Look for Plasmodium parasites.
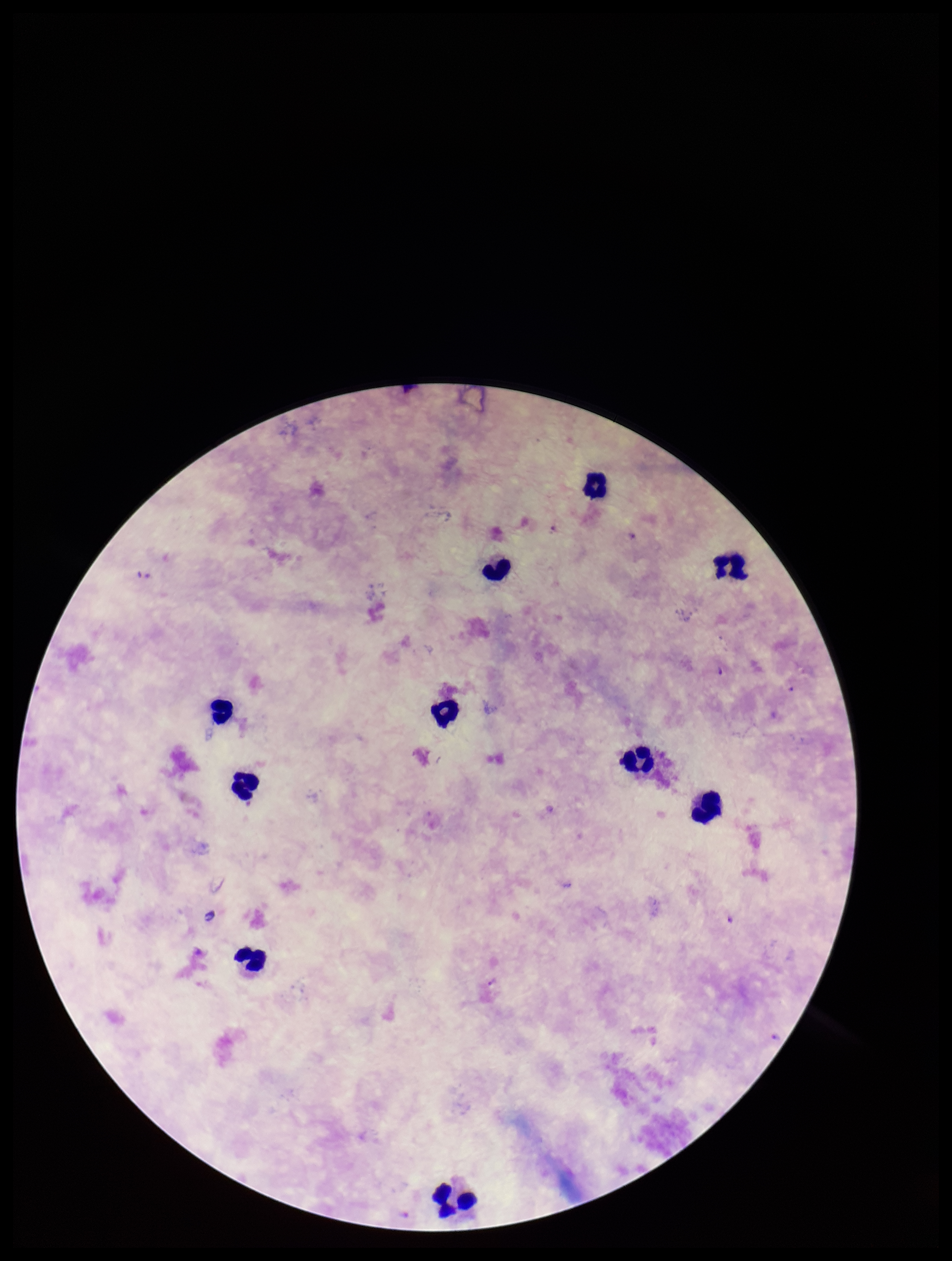

Identified.

Photographed through the microscope eyepiece with a smartphone camera. Species reported for this patient: Plasmodium falciparum. Single field of view. Parasite count: 1. Leukocyte count: 10. Image is 952×1261 pixels. Patient malaria status: positive. Giemsa stain. Preparation: thick smear.